Find each cell and give its type.
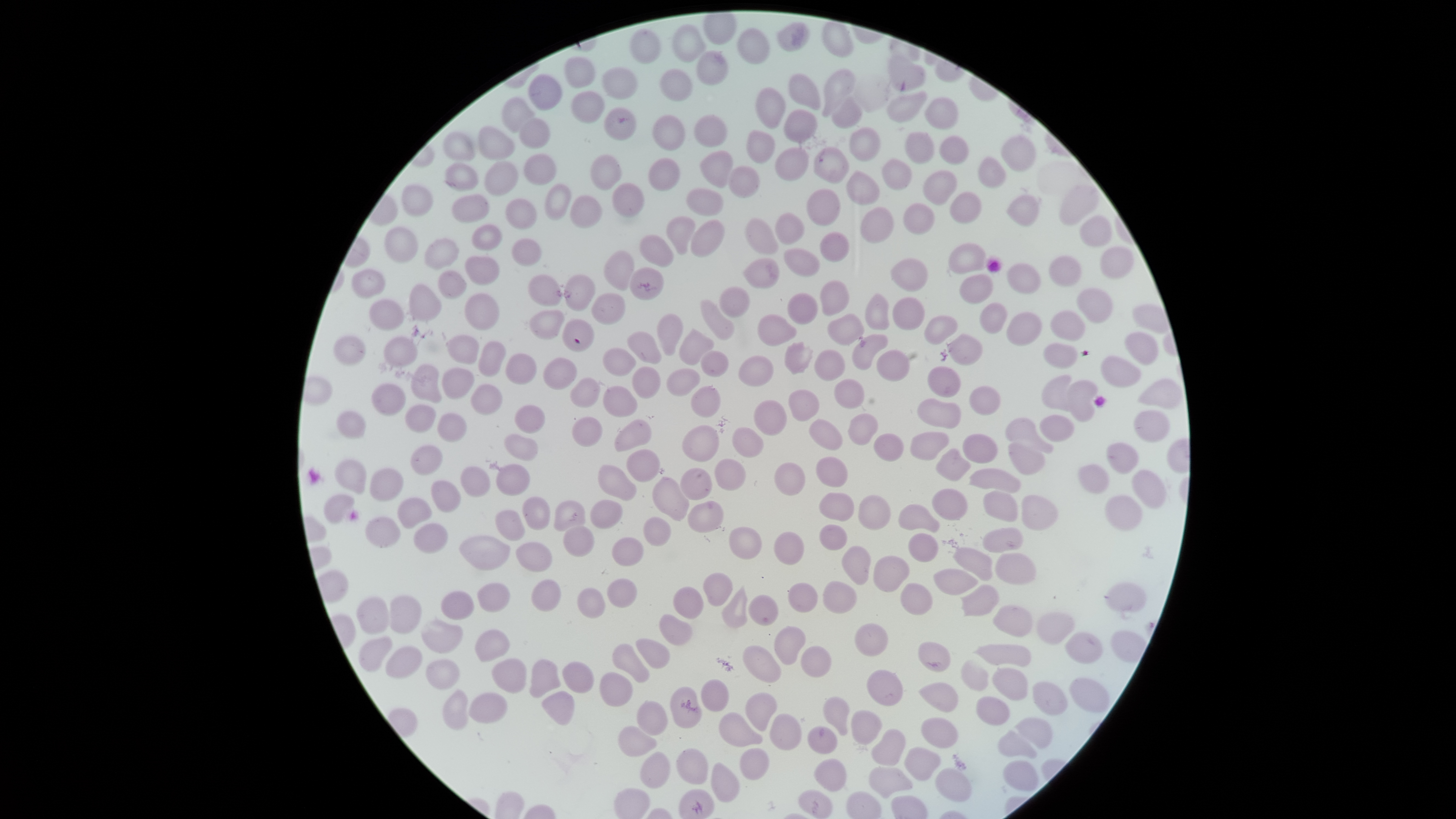
No parasitized red blood cells identified.
Approximate bounding boxes, in pixels from the top-left corner.
Uninfected red blood cells: (left=821, top=21, right=854, bottom=58), (left=671, top=24, right=705, bottom=62), (left=736, top=27, right=771, bottom=65), (left=629, top=28, right=661, bottom=65), (left=696, top=50, right=729, bottom=86), (left=888, top=54, right=926, bottom=91), (left=564, top=55, right=596, bottom=88), (left=601, top=66, right=638, bottom=100), (left=659, top=68, right=693, bottom=101), (left=822, top=68, right=855, bottom=117), (left=787, top=73, right=821, bottom=111), (left=528, top=74, right=562, bottom=111), (left=755, top=87, right=786, bottom=129), (left=886, top=90, right=928, bottom=123), (left=571, top=91, right=605, bottom=124), (left=501, top=96, right=535, bottom=133), (left=924, top=96, right=959, bottom=130), (left=832, top=98, right=861, bottom=129), (left=604, top=107, right=636, bottom=141), (left=782, top=109, right=818, bottom=143), (left=651, top=114, right=686, bottom=151), (left=692, top=114, right=729, bottom=147), (left=518, top=117, right=551, bottom=149), (left=478, top=126, right=516, bottom=160), (left=848, top=127, right=881, bottom=162), (left=746, top=129, right=775, bottom=164), (left=442, top=131, right=476, bottom=161), (left=905, top=131, right=935, bottom=164), (left=1001, top=134, right=1037, bottom=172), (left=939, top=135, right=969, bottom=164), (left=775, top=147, right=810, bottom=181), (left=813, top=147, right=850, bottom=184), (left=699, top=150, right=733, bottom=188), (left=523, top=154, right=557, bottom=186), (left=589, top=154, right=622, bottom=191), (left=978, top=155, right=1006, bottom=189), (left=647, top=157, right=680, bottom=191), (left=882, top=158, right=913, bottom=191), (left=444, top=161, right=479, bottom=192), (left=483, top=161, right=518, bottom=196), (left=728, top=165, right=760, bottom=198), (left=845, top=170, right=880, bottom=206), (left=923, top=170, right=957, bottom=205), (left=611, top=182, right=645, bottom=217), (left=401, top=183, right=434, bottom=217), (left=544, top=184, right=572, bottom=221), (left=1059, top=184, right=1099, bottom=226), (left=685, top=187, right=724, bottom=216), (left=806, top=188, right=841, bottom=226), (left=950, top=191, right=982, bottom=225), (left=451, top=193, right=490, bottom=224), (left=1007, top=194, right=1039, bottom=227), (left=569, top=195, right=602, bottom=229), (left=505, top=198, right=537, bottom=230), (left=903, top=203, right=935, bottom=235), (left=860, top=207, right=894, bottom=244), (left=774, top=212, right=805, bottom=245), (left=665, top=215, right=696, bottom=255), (left=1079, top=215, right=1113, bottom=247), (left=744, top=217, right=778, bottom=254), (left=690, top=219, right=725, bottom=258), (left=471, top=224, right=502, bottom=251), (left=383, top=226, right=418, bottom=263), (left=820, top=231, right=849, bottom=262), (left=639, top=234, right=675, bottom=267), (left=423, top=237, right=459, bottom=270), (left=511, top=238, right=543, bottom=266), (left=948, top=242, right=986, bottom=274), (left=1100, top=245, right=1134, bottom=279), (left=783, top=248, right=821, bottom=277), (left=603, top=250, right=635, bottom=292), (left=464, top=255, right=500, bottom=285), (left=1048, top=255, right=1082, bottom=287), (left=743, top=258, right=780, bottom=289), (left=890, top=258, right=928, bottom=292), (left=1005, top=262, right=1042, bottom=294), (left=628, top=267, right=664, bottom=300), (left=351, top=269, right=386, bottom=299), (left=437, top=270, right=467, bottom=299), (left=527, top=273, right=561, bottom=307), (left=564, top=274, right=596, bottom=312), (left=959, top=274, right=994, bottom=303), (left=819, top=280, right=850, bottom=316), (left=408, top=283, right=442, bottom=321), (left=718, top=285, right=750, bottom=318), (left=1076, top=287, right=1113, bottom=324), (left=590, top=292, right=626, bottom=325), (left=787, top=292, right=818, bottom=324), (left=464, top=293, right=500, bottom=331), (left=865, top=293, right=890, bottom=330), (left=893, top=296, right=925, bottom=330), (left=368, top=299, right=404, bottom=331), (left=699, top=299, right=735, bottom=340), (left=979, top=302, right=1008, bottom=334), (left=528, top=309, right=565, bottom=340), (left=1050, top=310, right=1085, bottom=342), (left=1006, top=312, right=1042, bottom=346), (left=657, top=313, right=684, bottom=356), (left=827, top=313, right=864, bottom=345), (left=757, top=314, right=797, bottom=346), (left=924, top=315, right=958, bottom=345), (left=561, top=318, right=594, bottom=352), (left=678, top=328, right=715, bottom=365), (left=627, top=331, right=662, bottom=365), (left=1124, top=331, right=1158, bottom=366), (left=851, top=333, right=889, bottom=371), (left=947, top=333, right=983, bottom=366), (left=333, top=335, right=366, bottom=365), (left=445, top=335, right=479, bottom=365), (left=383, top=337, right=418, bottom=367), (left=478, top=341, right=506, bottom=377), (left=783, top=341, right=813, bottom=375), (left=1043, top=343, right=1078, bottom=369), (left=602, top=346, right=636, bottom=377), (left=814, top=349, right=846, bottom=381), (left=876, top=349, right=910, bottom=382), (left=700, top=350, right=730, bottom=377), (left=505, top=353, right=537, bottom=385), (left=737, top=355, right=774, bottom=387), (left=1101, top=355, right=1142, bottom=388), (left=543, top=357, right=577, bottom=389), (left=410, top=364, right=442, bottom=403), (left=927, top=365, right=961, bottom=398), (left=632, top=366, right=661, bottom=399), (left=442, top=367, right=475, bottom=400), (left=666, top=368, right=701, bottom=396), (left=1041, top=374, right=1072, bottom=411), (left=570, top=377, right=601, bottom=408), (left=834, top=378, right=865, bottom=409), (left=1137, top=378, right=1183, bottom=410), (left=1068, top=380, right=1098, bottom=423), (left=371, top=383, right=406, bottom=416), (left=470, top=383, right=503, bottom=415), (left=690, top=385, right=721, bottom=417), (left=968, top=385, right=1001, bottom=416), (left=602, top=386, right=638, bottom=417), (left=788, top=389, right=820, bottom=422), (left=916, top=397, right=962, bottom=429), (left=753, top=399, right=788, bottom=436), (left=404, top=404, right=437, bottom=433), (left=514, top=405, right=546, bottom=434), (left=335, top=409, right=366, bottom=440), (left=1134, top=409, right=1170, bottom=442), (left=436, top=413, right=467, bottom=443), (left=848, top=413, right=878, bottom=446), (left=1039, top=414, right=1075, bottom=443), (left=572, top=416, right=602, bottom=447), (left=1004, top=417, right=1054, bottom=454), (left=808, top=418, right=843, bottom=450), (left=613, top=419, right=651, bottom=451), (left=681, top=424, right=719, bottom=462), (left=731, top=427, right=765, bottom=458), (left=909, top=431, right=949, bottom=462), (left=873, top=433, right=904, bottom=462), (left=962, top=433, right=998, bottom=464), (left=504, top=434, right=538, bottom=461), (left=1008, top=442, right=1046, bottom=475), (left=1106, top=442, right=1139, bottom=474), (left=410, top=444, right=443, bottom=475), (left=936, top=448, right=971, bottom=482), (left=626, top=449, right=661, bottom=482), (left=816, top=456, right=848, bottom=488), (left=714, top=458, right=746, bottom=491), (left=334, top=459, right=367, bottom=494), (left=774, top=462, right=806, bottom=496), (left=495, top=464, right=531, bottom=496), (left=1078, top=464, right=1110, bottom=494), (left=597, top=465, right=637, bottom=502), (left=460, top=466, right=491, bottom=497), (left=369, top=467, right=404, bottom=502), (left=679, top=467, right=713, bottom=501), (left=968, top=467, right=1021, bottom=494), (left=1132, top=469, right=1167, bottom=509), (left=652, top=476, right=690, bottom=521), (left=430, top=480, right=461, bottom=513), (left=931, top=489, right=968, bottom=521), (left=983, top=490, right=1018, bottom=522), (left=819, top=492, right=855, bottom=522), (left=323, top=494, right=355, bottom=524), (left=858, top=494, right=891, bottom=531), (left=1021, top=495, right=1059, bottom=531), (left=1104, top=495, right=1143, bottom=531), (left=522, top=496, right=551, bottom=530), (left=397, top=497, right=432, bottom=529), (left=589, top=499, right=624, bottom=529), (left=553, top=500, right=586, bottom=531), (left=687, top=501, right=724, bottom=533), (left=897, top=504, right=940, bottom=532), (left=494, top=510, right=524, bottom=541), (left=364, top=516, right=401, bottom=548), (left=642, top=516, right=672, bottom=547), (left=413, top=523, right=448, bottom=554), (left=818, top=524, right=848, bottom=551), (left=562, top=525, right=594, bottom=558), (left=728, top=526, right=763, bottom=559), (left=983, top=527, right=1024, bottom=553), (left=773, top=531, right=804, bottom=566), (left=908, top=533, right=939, bottom=563), (left=459, top=535, right=510, bottom=570), (left=611, top=537, right=644, bottom=567), (left=515, top=541, right=553, bottom=572), (left=841, top=545, right=871, bottom=585), (left=952, top=547, right=993, bottom=581), (left=995, top=553, right=1036, bottom=585), (left=872, top=555, right=911, bottom=593), (left=933, top=568, right=978, bottom=595), (left=702, top=572, right=733, bottom=607), (left=607, top=578, right=637, bottom=608), (left=531, top=579, right=561, bottom=612), (left=822, top=581, right=857, bottom=614), (left=477, top=582, right=510, bottom=613), (left=1104, top=582, right=1147, bottom=612), (left=787, top=583, right=818, bottom=613), (left=900, top=583, right=933, bottom=615), (left=961, top=584, right=1000, bottom=617), (left=672, top=586, right=704, bottom=620), (left=721, top=586, right=748, bottom=628), (left=577, top=588, right=606, bottom=619), (left=440, top=590, right=475, bottom=620), (left=389, top=595, right=421, bottom=634), (left=748, top=595, right=779, bottom=627), (left=356, top=596, right=389, bottom=634), (left=992, top=605, right=1033, bottom=638), (left=1036, top=612, right=1075, bottom=645), (left=659, top=614, right=693, bottom=646), (left=420, top=619, right=463, bottom=653), (left=854, top=623, right=888, bottom=657), (left=774, top=626, right=807, bottom=665), (left=475, top=629, right=510, bottom=662), (left=1064, top=631, right=1103, bottom=664), (left=358, top=635, right=393, bottom=672), (left=635, top=638, right=670, bottom=669), (left=917, top=641, right=951, bottom=673), (left=972, top=643, right=1032, bottom=667), (left=612, top=644, right=649, bottom=683), (left=385, top=645, right=423, bottom=679), (left=742, top=646, right=781, bottom=683), (left=801, top=646, right=832, bottom=678), (left=491, top=658, right=527, bottom=694), (left=529, top=659, right=561, bottom=698), (left=960, top=659, right=989, bottom=692), (left=425, top=660, right=459, bottom=690), (left=562, top=661, right=594, bottom=693), (left=991, top=667, right=1028, bottom=701), (left=866, top=669, right=903, bottom=706), (left=599, top=671, right=633, bottom=707), (left=701, top=678, right=730, bottom=712), (left=1069, top=678, right=1109, bottom=713), (left=1032, top=681, right=1068, bottom=716), (left=918, top=682, right=959, bottom=712), (left=670, top=686, right=702, bottom=728), (left=442, top=688, right=470, bottom=731), (left=468, top=692, right=508, bottom=724), (left=541, top=692, right=575, bottom=726), (left=745, top=692, right=778, bottom=731), (left=823, top=696, right=850, bottom=736), (left=976, top=696, right=1010, bottom=726), (left=636, top=701, right=668, bottom=735), (left=850, top=710, right=881, bottom=745), (left=718, top=712, right=763, bottom=747), (left=769, top=713, right=802, bottom=751), (left=920, top=717, right=958, bottom=748), (left=1014, top=717, right=1053, bottom=749), (left=617, top=725, right=657, bottom=757), (left=807, top=725, right=838, bottom=754), (left=871, top=728, right=905, bottom=766), (left=997, top=730, right=1038, bottom=759), (left=904, top=747, right=941, bottom=781), (left=675, top=748, right=709, bottom=785), (left=739, top=748, right=770, bottom=780), (left=639, top=751, right=670, bottom=789), (left=813, top=758, right=846, bottom=792), (left=1002, top=760, right=1039, bottom=791), (left=711, top=762, right=740, bottom=803), (left=868, top=766, right=913, bottom=799), (left=935, top=768, right=972, bottom=802), (left=798, top=789, right=834, bottom=819).
No white blood cells identified.

Summary:
  - Capture: smartphone photograph through the microscope eyepiece
  - Visible region: circular
  - Field of view: single
  - Preparation: thin blood smear
  - Image size: 1456×819 pixels
  - Stain: Giemsa